Name the parasite shown.
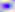
Toxoplasma gondii.

magnification = 400x
modality = micrograph